Identify the preparation type.
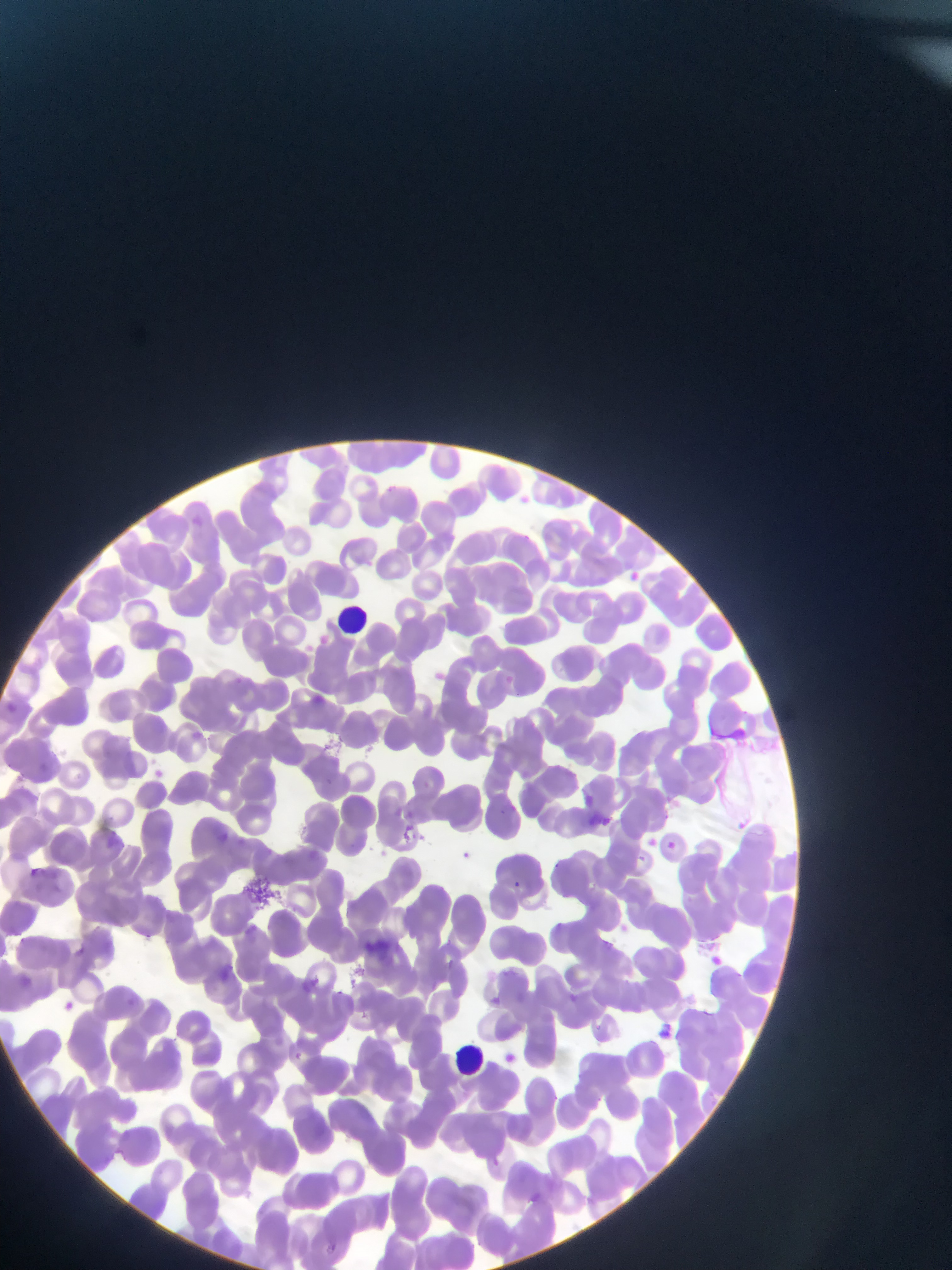
Thin blood smear.

Plasmodium parasite locations = approximate bounding boxes as [left, top, right, bottom] in pixels: [630, 568, 647, 592], [320, 633, 340, 656], [436, 672, 452, 684], [233, 675, 245, 687], [505, 676, 513, 683], [313, 693, 348, 714], [4, 696, 24, 716], [193, 730, 203, 749], [38, 756, 57, 774], [153, 763, 168, 776], [581, 789, 599, 806], [506, 802, 531, 819], [393, 803, 401, 813], [406, 804, 417, 819], [592, 812, 613, 829], [732, 813, 752, 838], [402, 821, 419, 845], [218, 823, 235, 842], [649, 831, 662, 852], [668, 843, 674, 851], [459, 847, 479, 863], [25, 860, 47, 877], [509, 880, 526, 888], [79, 941, 91, 954], [712, 953, 723, 968], [489, 989, 515, 1010], [63, 998, 87, 1013], [657, 1016, 676, 1040], [496, 1046, 522, 1062], [528, 1180, 546, 1202], [329, 1237, 341, 1249]
field of view = single
country = Ghana
capture = mobile-phone photograph through a microscope
leukocyte locations = approximate bounding boxes as [left, top, right, bottom] in pixels: [335, 603, 370, 631], [454, 1039, 481, 1073]
image size = 952×1270 pixels